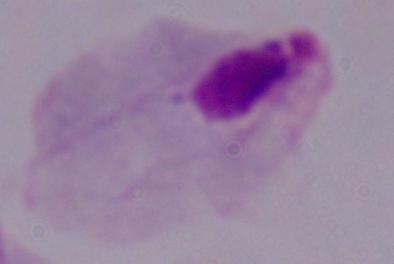
A trichomonad is seen. Photomicrograph. 1000x magnification.